Point out each leukocyte.
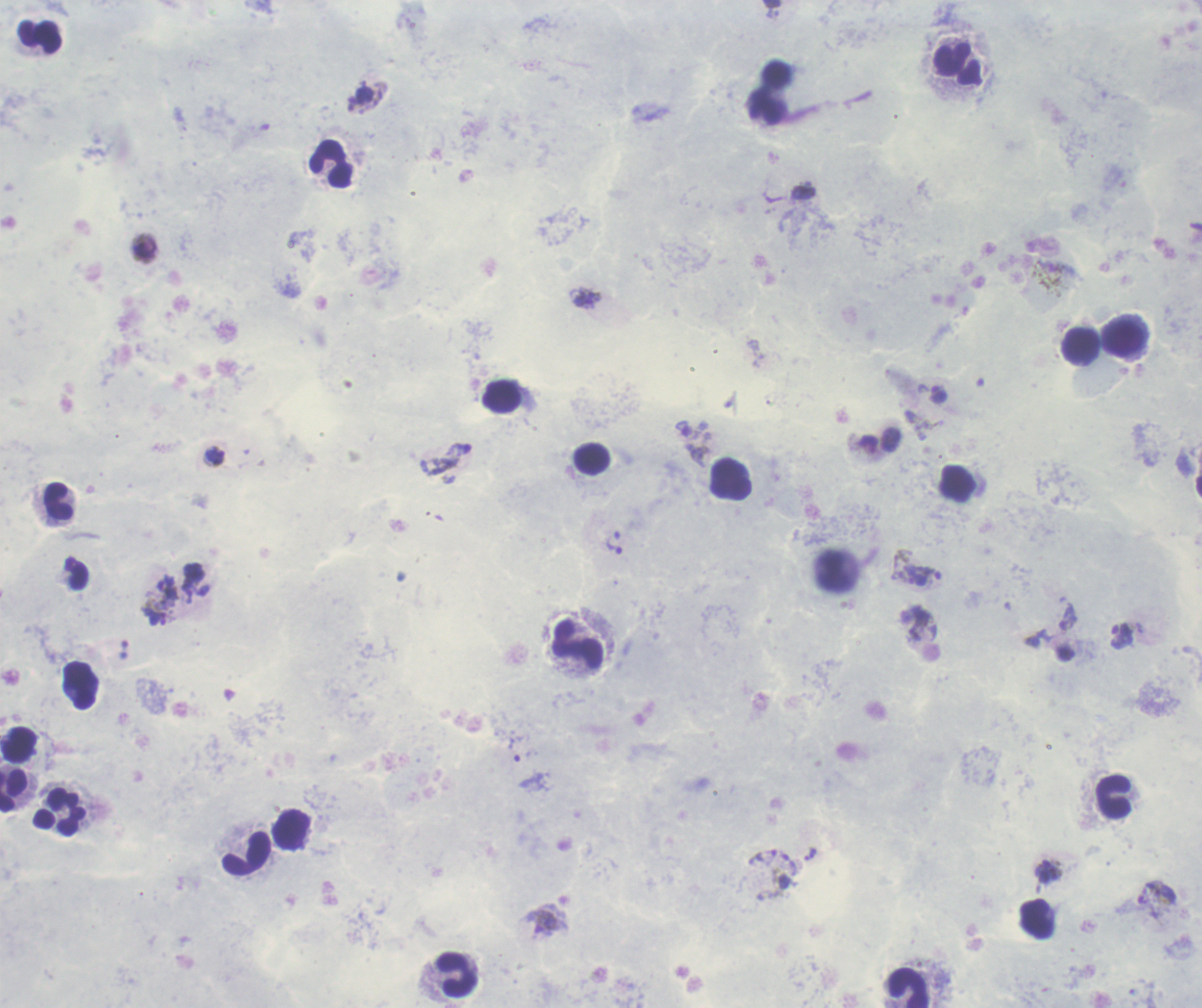

Approximate centers as [x, y] in pixels.
Leukocytes: [40, 37], [957, 64], [331, 163], [1124, 339], [1082, 345], [502, 397], [592, 458], [732, 480], [58, 502], [578, 645], [81, 685], [19, 745], [13, 791], [1114, 797], [60, 813], [291, 830], [248, 854], [1037, 918], [458, 975], [908, 988].

Approximate centers as [x, y] in pixels.
Summary:
  - Trophozoite locations: [587, 299], [938, 395], [214, 456], [168, 591], [1122, 635], [514, 749], [1048, 871]
  - Gametocyte locations: [695, 446], [1068, 616], [542, 923]
  - Life-cycle stages observed: trophozoite, gametocyte
  - Image size: 1202×1008 pixels
  - Result: Plasmodium parasites identified
  - Preparation: thick blood smear
  - Stain: Romanowsky
  - Field of view: one from this slide
  - Context: previously used in an actual diagnosis
  - Background quality: poor
  - Magnification: 100x
  - Coloration quality: good